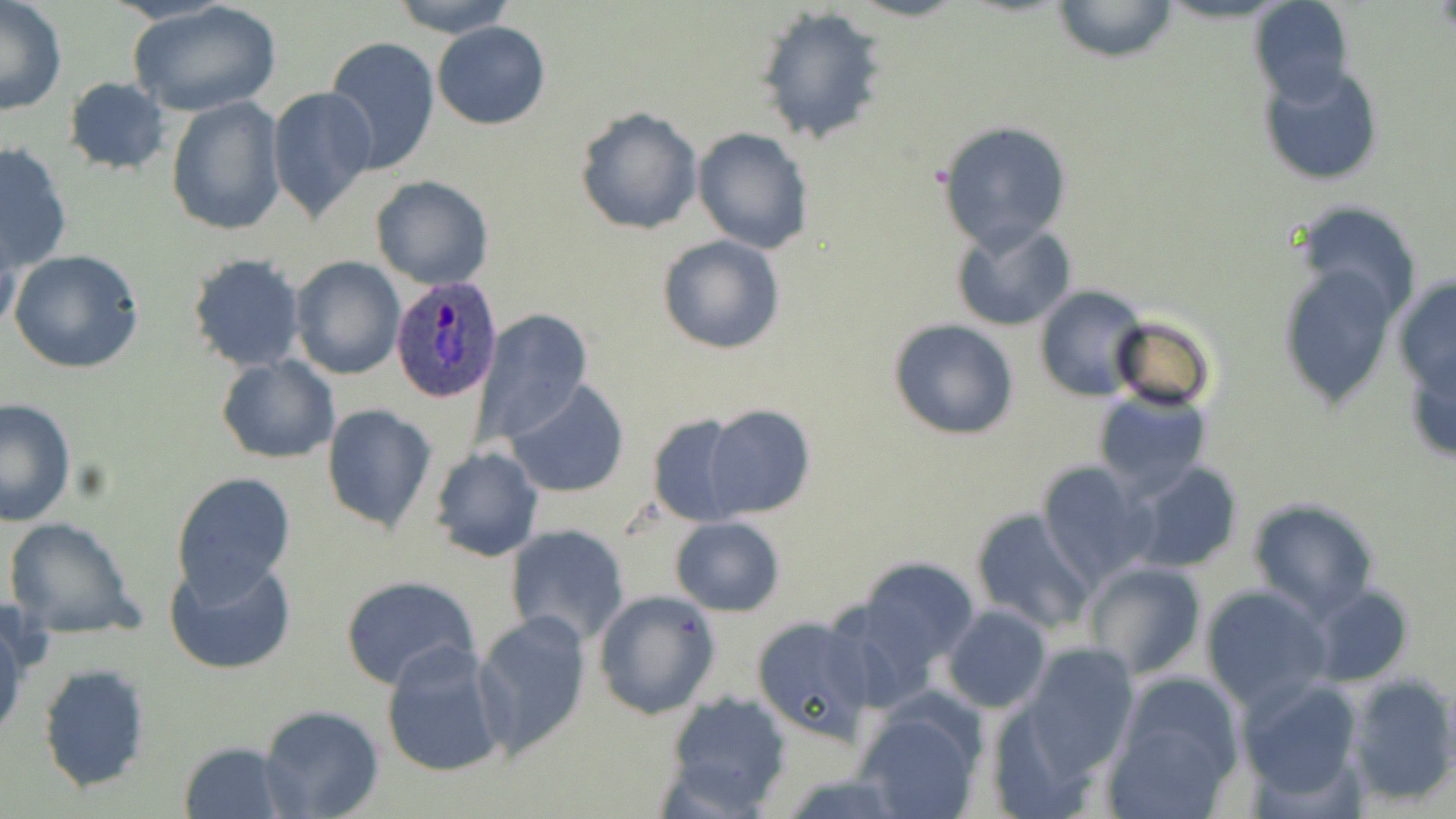

slide-level diagnosis = Plasmodium ovale
image size = 1456×819 pixels
preparation = thin blood film
stain = May-Grünwald-Giemsa
Plasmodium ovale-infected red blood cell locations = approximate bounding boxes as [x1, y1, x2, y2] in pixels: [390, 280, 502, 401]
magnification = 1000x
field of view = single
uninfected red blood cell locations = approximate bounding boxes as [x1, y1, x2, y2] in pixels: [128, 0, 282, 118], [391, 0, 518, 39], [1051, 0, 1179, 64], [1249, 0, 1354, 104], [0, 1, 68, 116], [756, 5, 890, 146], [431, 22, 551, 129], [325, 36, 440, 179], [1259, 64, 1384, 188], [64, 76, 170, 176], [267, 85, 379, 226], [166, 97, 285, 236], [575, 106, 704, 235], [938, 122, 1072, 251], [693, 127, 813, 254], [1, 142, 73, 271], [370, 175, 494, 290], [1291, 199, 1424, 326], [1, 216, 24, 339], [949, 220, 1077, 332], [655, 234, 785, 356], [8, 249, 147, 375], [186, 253, 305, 372], [290, 256, 405, 381], [1276, 262, 1401, 410], [1393, 276, 1456, 402], [1035, 285, 1149, 401], [474, 308, 593, 447], [1108, 315, 1215, 413], [887, 318, 1022, 440], [216, 354, 340, 462], [506, 380, 629, 499], [1093, 389, 1214, 498], [0, 398, 76, 526], [701, 403, 815, 519], [321, 404, 437, 535], [646, 414, 754, 526], [429, 446, 544, 561], [1036, 461, 1156, 586], [1127, 461, 1245, 573], [174, 471, 295, 599], [1247, 496, 1380, 619], [969, 507, 1094, 633], [5, 517, 144, 639], [670, 517, 785, 616], [505, 524, 631, 648], [165, 553, 299, 675], [851, 554, 982, 677], [1083, 562, 1207, 679], [339, 574, 482, 689], [1199, 586, 1330, 712], [1309, 586, 1415, 685], [593, 590, 719, 719], [942, 606, 1052, 713], [0, 608, 26, 747], [471, 612, 593, 759], [751, 615, 878, 744], [380, 641, 508, 779], [1021, 644, 1137, 778], [37, 661, 151, 793], [1107, 671, 1244, 816], [1346, 672, 1456, 806], [1237, 676, 1367, 804], [663, 691, 793, 812], [258, 707, 384, 819], [855, 707, 984, 819], [178, 739, 291, 818]
modality = optical microscopy